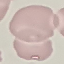

malaria status = uninfected
preparation = thin blood film
capture = smartphone through the microscope eyepiece
stain = Giemsa
image type = cell patch, automatically extracted from a larger field of view and resized to 64 × 64 pixels